Locate every Plasmodium parasite.
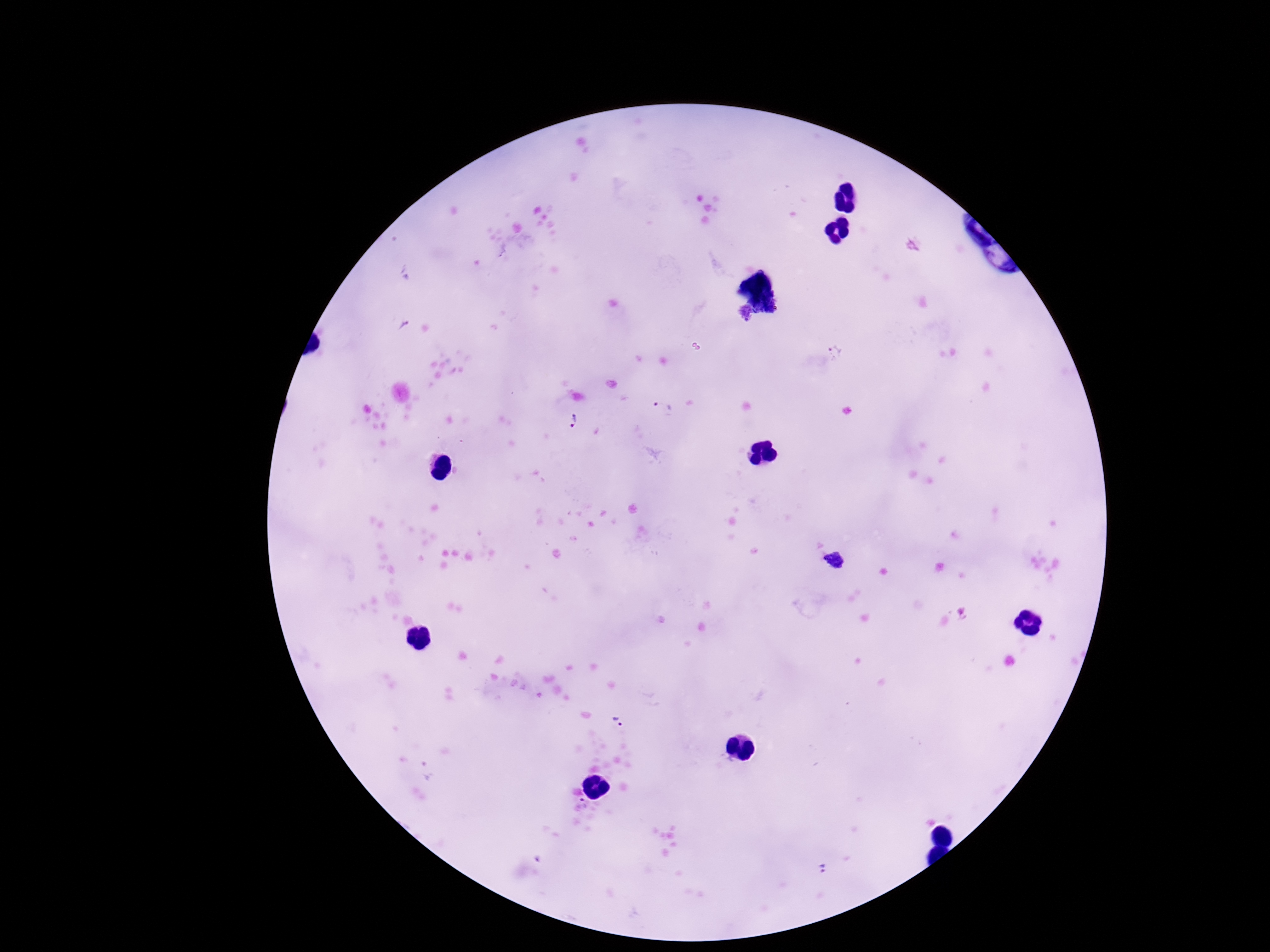

Approximate centers as {x, y} in pixels.
Plasmodium parasites: {836, 350}, {663, 407}, {569, 424}, {836, 562}, {617, 723}, {821, 868}.

Giemsa-stained preparation. Image is 1270×952 pixels. 100x magnification. Single field of view. Thick peripheral-blood smear. Smartphone photograph taken through the microscope eyepiece. Patient malaria status: infected.